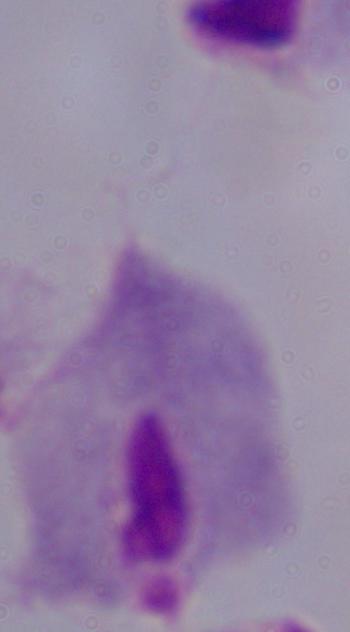

Summary:
  - Modality: micrograph
  - Magnification: 1000x
  - Identification: trichomonad